Locate every malaria parasite.
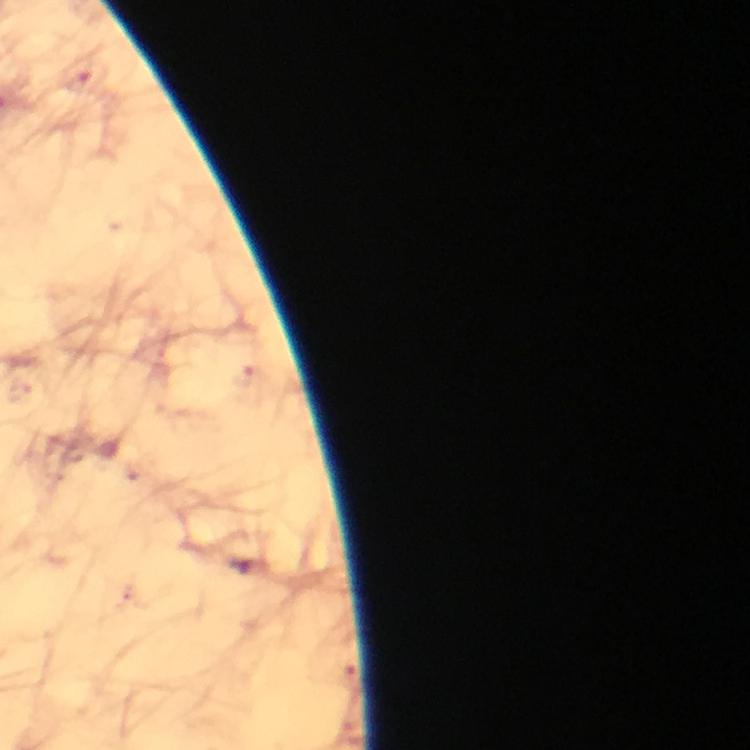

Approximate centers as (x, y) in pixels.
Malaria parasites: (77, 79).

From a diagnostic examination for malaria. 100x magnification. Giemsa-stained preparation. Thick smear. Immersion oil applied. Smartphone photograph taken through a microscope. A crop from one field of view. Image is 750×750 pixels.